Name the parasite shown.
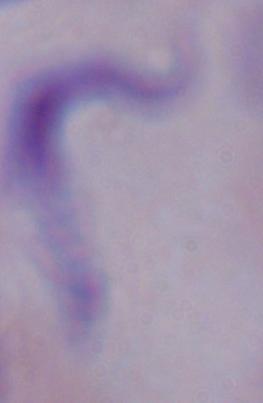

This is a trypanosome.

{
  "magnification": "1000x",
  "modality": "photomicrograph"
}